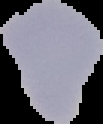

Summary:
  - Image size: 103×124 pixels
  - Malaria status: parasitized
  - Image type: cell region segmented out of the field of view; surrounding area masked to black
  - Preparation: thin blood film